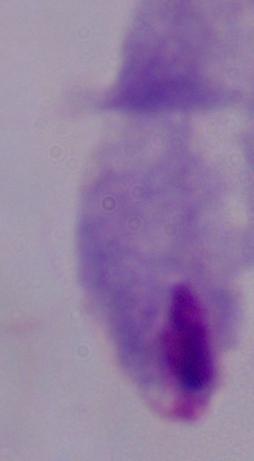
identification: trichomonad
modality: photomicrograph
magnification: 1000x